Comment on the morphology of the erythrocytes.
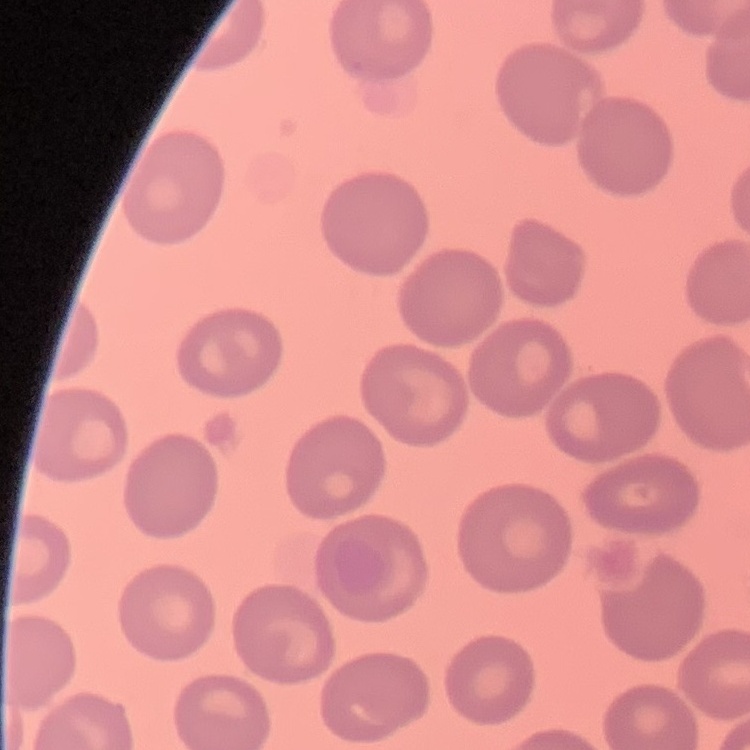
They show no rouleaux formation.

preparation = thin blood smear
image type = one tile cut from a larger photomicrograph
stain = Field's or Giemsa